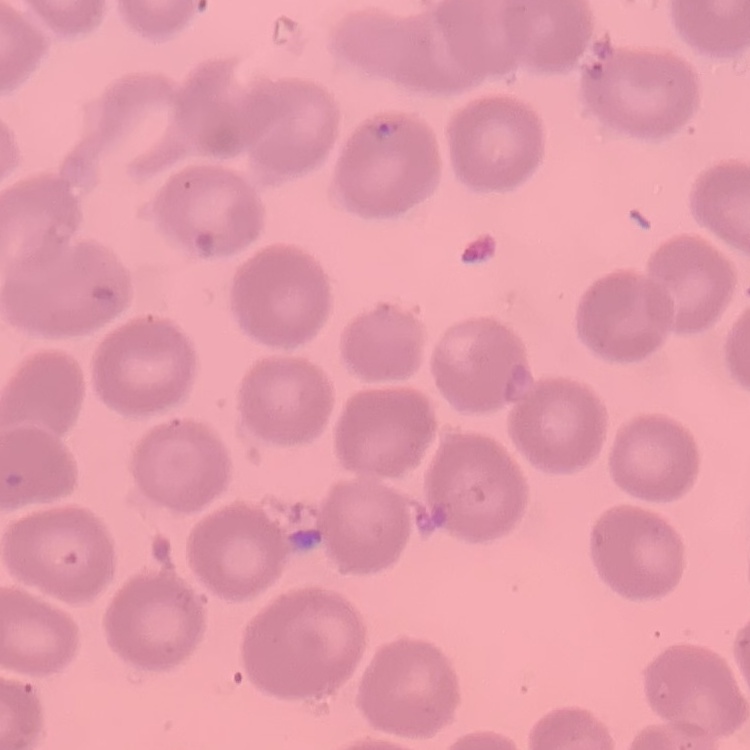

erythrocyte morphology = no rouleaux formation
stain = Field's or Giemsa
image type = one tile cut from a larger photomicrograph
preparation = thin blood smear